Name the cell type shown.
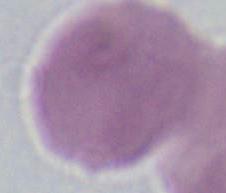

This is an erythrocyte.

Summary:
  - Magnification: 1000x
  - Modality: photomicrograph